Locate every Plasmodium falciparum-infected red blood cell.
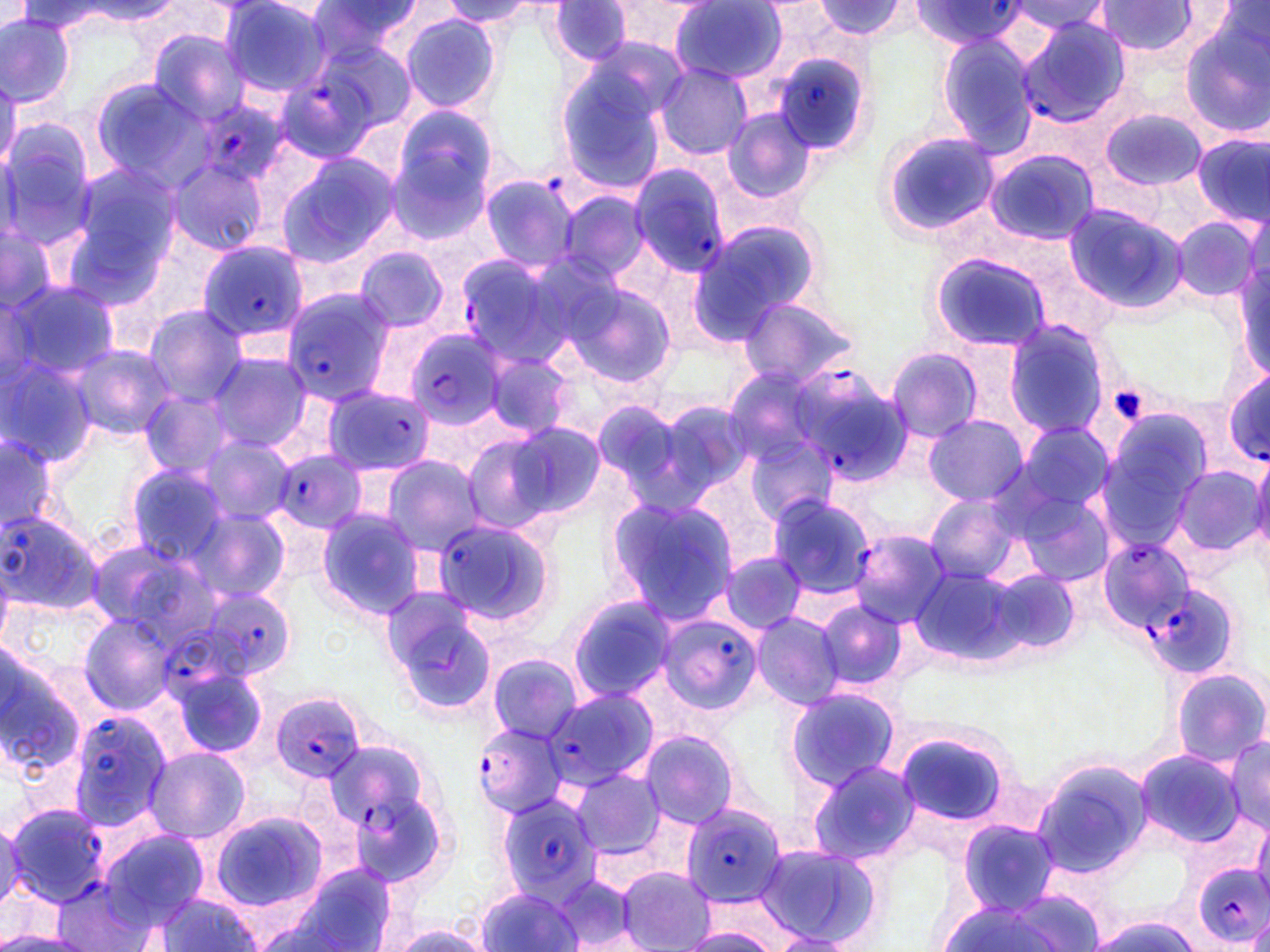

Approximate bounding boxes as (x1,y1)-(x2,y2) corner pairs in pixels.
Plasmodium falciparum-infected red blood cells: (909,2)-(1030,47), (1014,15)-(1136,127), (770,53)-(875,155), (274,73)-(376,161), (196,95)-(292,188), (627,163)-(730,274), (198,239)-(313,345), (452,251)-(577,365), (279,287)-(393,402), (404,327)-(508,431), (790,361)-(910,486), (1221,367)-(1270,471), (322,387)-(437,476), (273,449)-(366,533), (0,506)-(104,616), (430,515)-(561,637), (846,529)-(950,628), (1097,537)-(1194,632), (1145,581)-(1241,677), (199,589)-(296,680), (656,612)-(764,715), (158,631)-(260,712), (539,690)-(658,789), (270,693)-(368,782), (64,711)-(170,832), (472,722)-(572,821), (330,743)-(424,841), (495,794)-(603,901), (681,801)-(790,907), (3,803)-(108,906), (1193,863)-(1270,947).

slide_level_diagnosis: Plasmodium falciparum
image_size: 1270×952 pixels
modality: optical microscopy
magnification: 1000x
preparation: thin blood film
uninfected_red_blood_cell_locations: 'approximate bounding boxes as (x1,y1)-(x2,y2) corner pairs in pixels: (219,1)-(331,98), (303,1)-(420,65), (440,1)-(544,27), (672,1)-(791,84), (815,1)-(909,40), (1096,1)-(1197,56), (17,2)-(136,34), (72,2)-(179,24), (549,2)-(634,67), (1008,2)-(1113,37), (0,13)-(77,109), (400,13)-(502,114), (1180,21)-(1270,138), (149,29)-(251,126), (935,30)-(1041,156), (312,37)-(418,138), (552,55)-(674,198), (657,64)-(753,160), (88,78)-(208,189), (0,81)-(20,176), (389,104)-(503,225), (1100,106)-(1206,191), (721,107)-(819,207), (0,124)-(96,249), (877,130)-(998,240), (1190,132)-(1270,228), (985,149)-(1099,246), (275,153)-(398,268), (167,159)-(267,256), (66,161)-(183,278), (479,173)-(578,272), (557,190)-(652,283), (1063,205)-(1188,314), (1172,216)-(1261,302), (689,221)-(820,339), (0,223)-(63,316), (354,248)-(449,333), (931,253)-(1054,352), (1235,255)-(1269,385), (4,278)-(122,383), (567,281)-(679,389), (736,294)-(860,388), (140,305)-(249,405), (1002,321)-(1112,441), (69,343)-(176,439), (884,346)-(983,444), (0,350)-(98,466), (481,350)-(579,441), (207,352)-(314,454), (722,368)-(827,468), (138,389)-(237,479), (588,398)-(710,515), (656,400)-(755,499), (923,414)-(1027,507), (1093,417)-(1210,552), (502,420)-(608,521), (1012,421)-(1115,521), (0,431)-(60,535), (744,432)-(838,530), (460,433)-(564,532), (195,437)-(294,526), (1248,450)-(1270,558), (381,456)-(483,555), (123,464)-(231,565), (1169,464)-(1266,558), (1010,484)-(1118,589), (922,493)-(1027,585), (767,494)-(876,599), (605,495)-(739,622), (189,506)-(292,604), (315,508)-(423,619), (85,537)-(211,635), (719,550)-(808,636), (906,562)-(1032,668), (985,569)-(1083,655), (378,587)-(494,713), (567,596)-(677,703), (817,600)-(907,691), (750,610)-(845,709), (78,612)-(178,715), (0,649)-(89,770), (487,655)-(581,743), (168,663)-(269,760), (1170,666)-(1269,768), (784,688)-(901,792), (891,727)-(1018,832), (637,729)-(741,830), (1224,734)-(1270,833), (143,746)-(251,844), (1134,750)-(1246,849), (805,759)-(923,866), (1028,759)-(1154,881), (568,769)-(665,858), (211,811)-(328,913), (1250,818)-(1270,903), (958,820)-(1058,913), (97,828)-(210,933), (754,842)-(883,950), (286,864)-(400,950), (616,866)-(715,952), (549,874)-(640,947), (54,878)-(151,952), (474,886)-(586,952), (152,894)-(265,951), (934,899)-(1073,951), (242,911)-(361,952), (1082,913)-(1204,951), (378,920)-(491,952), (674,925)-(779,951), (0,930)-(92,952), (768,932)-(855,951)'
stain: May-Grünwald-Giemsa
field_of_view: one of a larger specimen
platelet_locations: 'approximate bounding boxes as (x1,y1)-(x2,y2) corner pairs in pixels: (1107,384)-(1151,426)'